Give the position of every Plasmodium parasite.
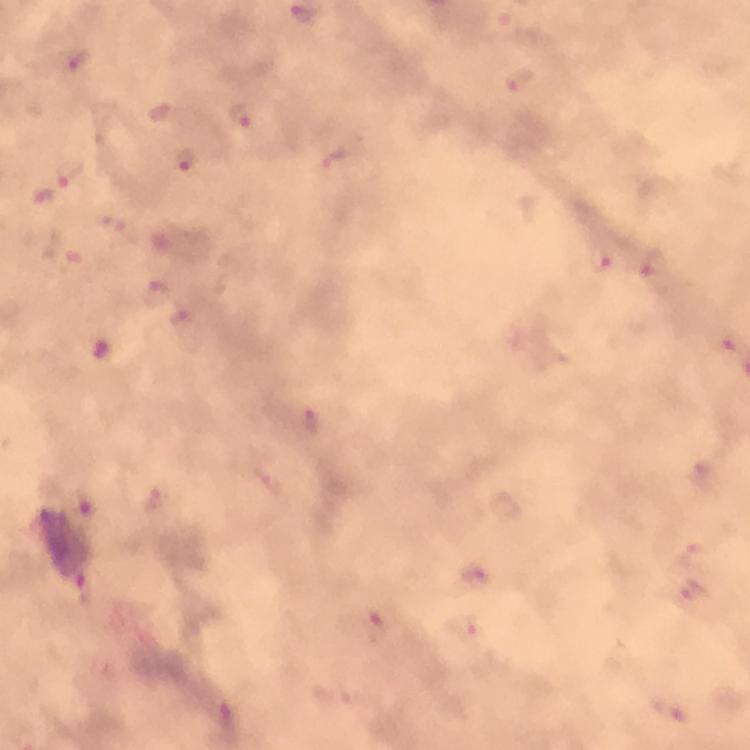

Approximate object centers, in pixels from the top-left corner.
Plasmodium parasites: (x=72, y=61), (x=239, y=115), (x=186, y=159), (x=72, y=174), (x=601, y=261), (x=475, y=577), (x=693, y=589).

stain: Giemsa
immersion_oil: used
preparation: thick blood film
image_size: 750×750 pixels
cropped_from: one field of view
context: from a malaria diagnostic workup
magnification: 100x
capture: smartphone mounted on the microscope